Name the blood parasite species.
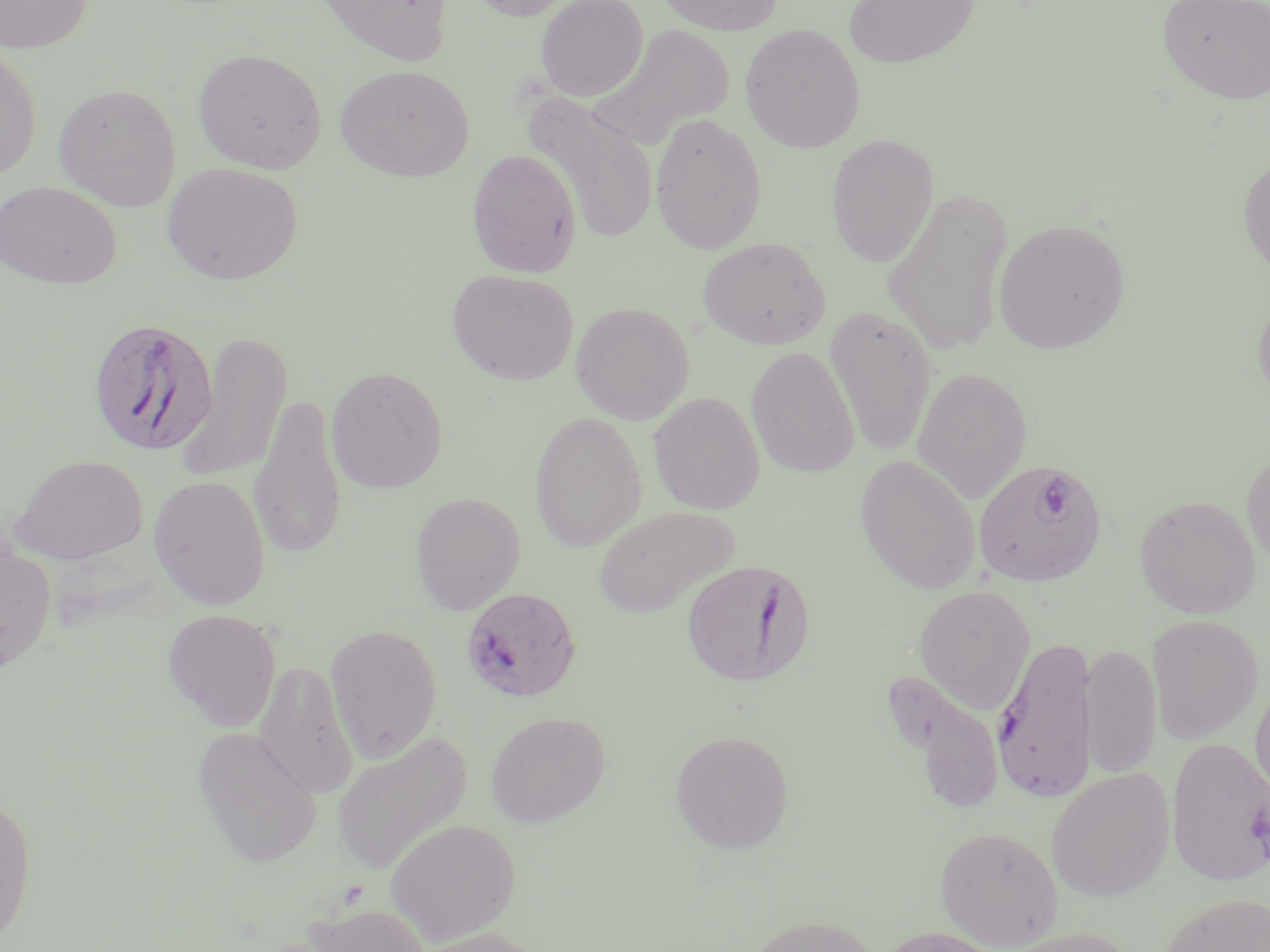
Plasmodium falciparum.

{
  "stain": "May-Grünwald-Giemsa",
  "field_of_view": "single",
  "modality": "optical microscopy",
  "magnification": "1000x",
  "plasmodium_falciparum_infected_red_blood_cell_locations": "approximate bounding boxes as named x1/y1/x2/y2 corners in pixels: (x1=87, y1=317, x2=218, y2=458), (x1=973, y1=460, x2=1108, y2=587), (x1=681, y1=558, x2=813, y2=687), (x1=462, y1=587, x2=581, y2=703), (x1=992, y1=633, x2=1098, y2=803), (x1=1166, y1=737, x2=1270, y2=887)",
  "image_size": "1270×952 pixels",
  "uninfected_red_blood_cell_locations": "approximate bounding boxes as named x1/y1/x2/y2 corners in pixels: (x1=0, y1=0, x2=93, y2=54), (x1=316, y1=0, x2=454, y2=68), (x1=464, y1=0, x2=580, y2=22), (x1=535, y1=0, x2=649, y2=101), (x1=655, y1=0, x2=785, y2=35), (x1=843, y1=0, x2=980, y2=69), (x1=1156, y1=0, x2=1270, y2=106), (x1=594, y1=23, x2=735, y2=146), (x1=740, y1=24, x2=866, y2=153), (x1=0, y1=45, x2=41, y2=182), (x1=192, y1=48, x2=327, y2=173), (x1=335, y1=63, x2=475, y2=181), (x1=53, y1=83, x2=181, y2=212), (x1=521, y1=92, x2=659, y2=244), (x1=649, y1=111, x2=767, y2=254), (x1=826, y1=134, x2=939, y2=267), (x1=466, y1=148, x2=582, y2=278), (x1=1237, y1=154, x2=1270, y2=282), (x1=161, y1=161, x2=303, y2=285), (x1=0, y1=181, x2=122, y2=289), (x1=881, y1=188, x2=1014, y2=357), (x1=993, y1=218, x2=1130, y2=354), (x1=697, y1=236, x2=831, y2=350), (x1=447, y1=269, x2=578, y2=386), (x1=1252, y1=286, x2=1270, y2=411), (x1=570, y1=301, x2=694, y2=425), (x1=824, y1=306, x2=938, y2=458), (x1=176, y1=331, x2=293, y2=487), (x1=746, y1=346, x2=860, y2=479), (x1=325, y1=366, x2=449, y2=493), (x1=911, y1=367, x2=1032, y2=504), (x1=648, y1=392, x2=765, y2=515), (x1=248, y1=393, x2=348, y2=562), (x1=529, y1=411, x2=647, y2=552), (x1=1241, y1=444, x2=1270, y2=572), (x1=10, y1=454, x2=149, y2=565), (x1=855, y1=454, x2=981, y2=594), (x1=148, y1=474, x2=270, y2=610), (x1=410, y1=491, x2=526, y2=615), (x1=1136, y1=496, x2=1262, y2=620), (x1=593, y1=505, x2=739, y2=619), (x1=0, y1=536, x2=57, y2=675), (x1=914, y1=585, x2=1036, y2=716), (x1=162, y1=609, x2=282, y2=732), (x1=1147, y1=614, x2=1264, y2=745), (x1=325, y1=624, x2=442, y2=761), (x1=1080, y1=641, x2=1162, y2=782), (x1=254, y1=661, x2=360, y2=799), (x1=884, y1=673, x2=1004, y2=811), (x1=1249, y1=673, x2=1270, y2=813), (x1=486, y1=711, x2=611, y2=827), (x1=192, y1=726, x2=323, y2=868), (x1=331, y1=729, x2=473, y2=875), (x1=670, y1=729, x2=794, y2=855), (x1=1047, y1=768, x2=1175, y2=902), (x1=0, y1=791, x2=38, y2=945), (x1=385, y1=817, x2=520, y2=944), (x1=935, y1=825, x2=1064, y2=949), (x1=1156, y1=892, x2=1270, y2=952), (x1=306, y1=903, x2=434, y2=952), (x1=742, y1=914, x2=882, y2=952), (x1=412, y1=926, x2=553, y2=952), (x1=875, y1=926, x2=1010, y2=952), (x1=998, y1=927, x2=1140, y2=952)",
  "preparation": "thin blood smear"
}